Comment on the morphology of the erythrocytes.
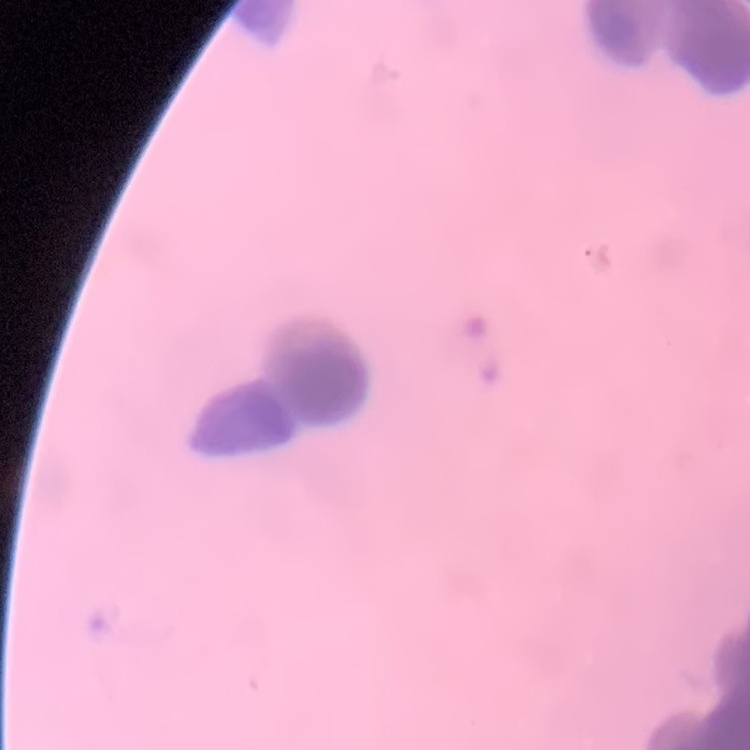
Rouleaux formation.

Summary:
  - Image type: square crop of a larger photomicrograph
  - Stain: Field's or Giemsa
  - Preparation: thin blood smear